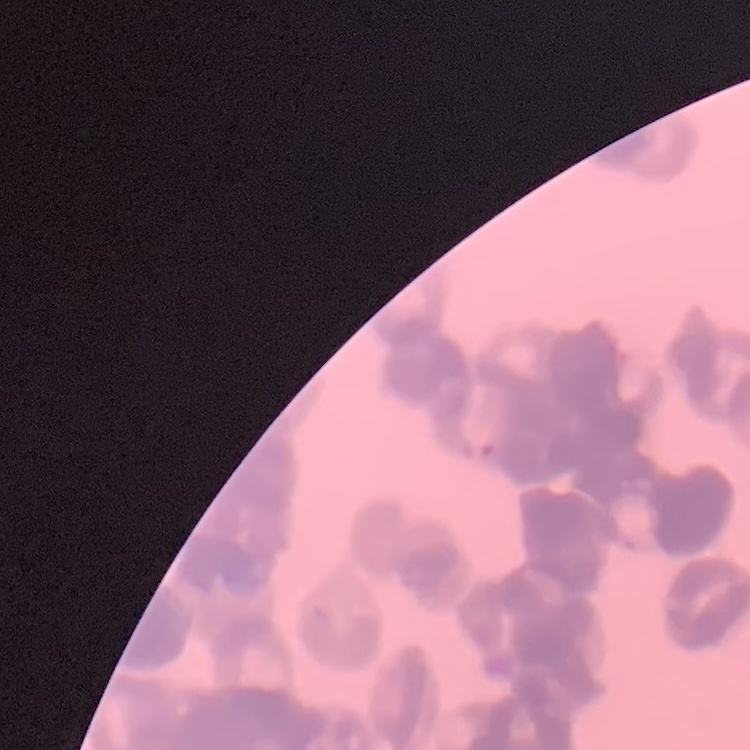
The erythrocytes exhibit rouleaux formation. One tile cut from a larger photomicrograph. Thin blood smear. Stained with either Field's or Giemsa.